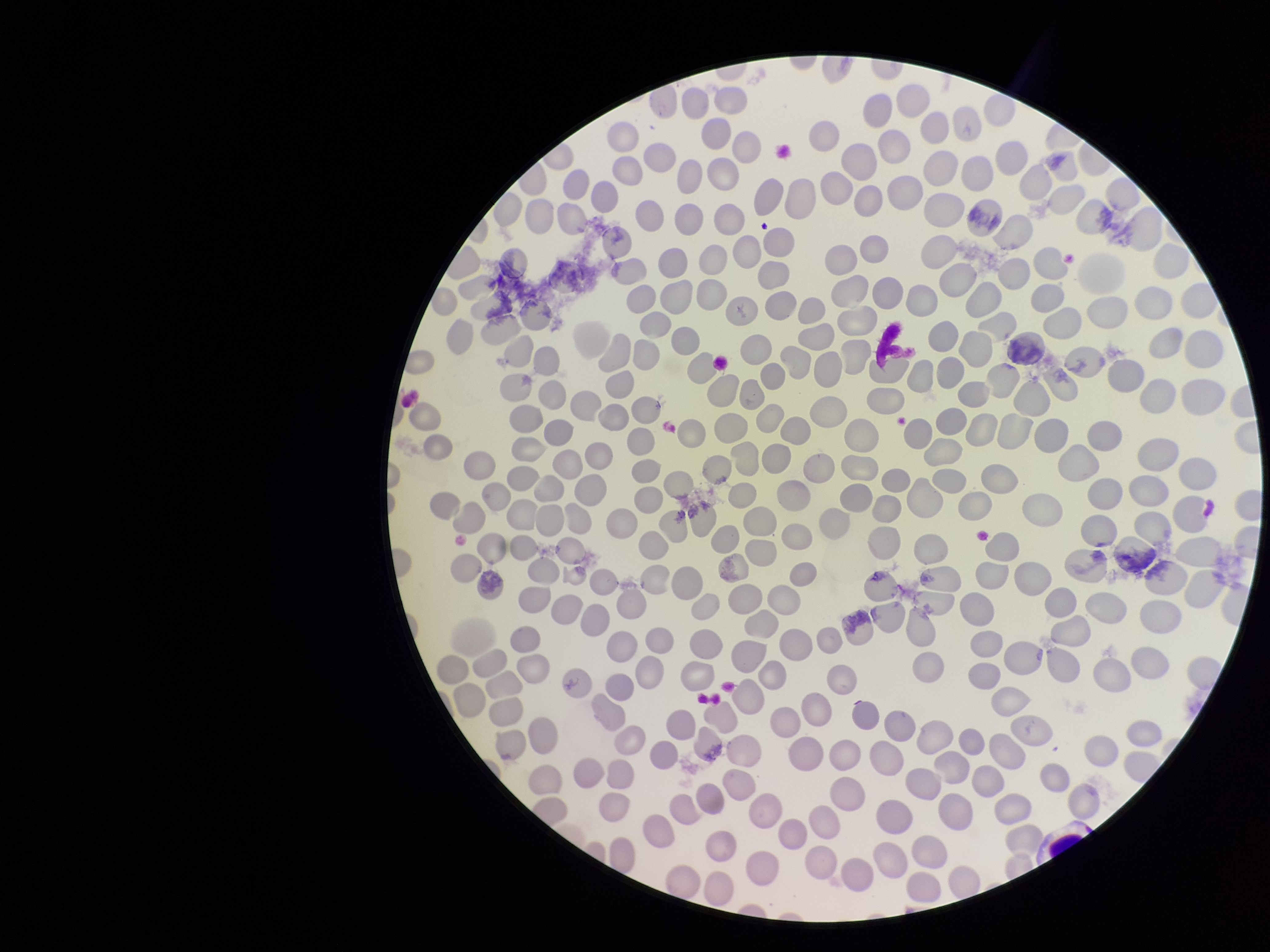
Summary:
  - Parasitized red blood cell count: 0
  - Red blood cell count: 319
  - Stain: Giemsa
  - Parasitized red blood cells: none identified
  - Preparation: thin blood smear
  - Species reported for this patient: Plasmodium falciparum
  - Capture: smartphone photograph through the microscope eyepiece
  - Field of view: single
  - Patient malaria status: positive
  - Image size: 1270×952 pixels